Assess this cell for malaria.
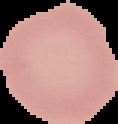
Uninfected.

image type = segmented cell region with the area outside set to black
image size = 118×124 pixels
preparation = thin blood smear